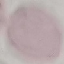

Result: no malaria parasites detected. Automatically extracted cell patch, resized to 64 × 64 pixels. Thin blood film. Giemsa stain. Photographed with a smartphone camera at the microscope eyepiece.